Report the malaria status of this cell.
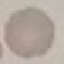

It is uninfected.

Cell patch, automatically extracted from a larger field of view and resized to 64 × 64 pixels. Thin blood film. Acquired by smartphone through the microscope eyepiece. Giemsa-stained preparation.